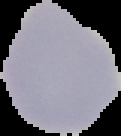

{
  "image_type": "segmented cell region with the area outside set to black",
  "image_size": "121×136 pixels",
  "preparation": "thin blood smear",
  "malaria_status": "uninfected"
}